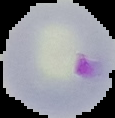
image size = 115×118 pixels
image type = segmented cell region on a black background
preparation = thin blood film
malaria status = parasitized